Report the malaria status of this cell.
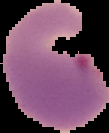
Parasitized.

image type = cell region segmented out of the field of view; surrounding area masked to black
image size = 109×133 pixels
preparation = thin blood film